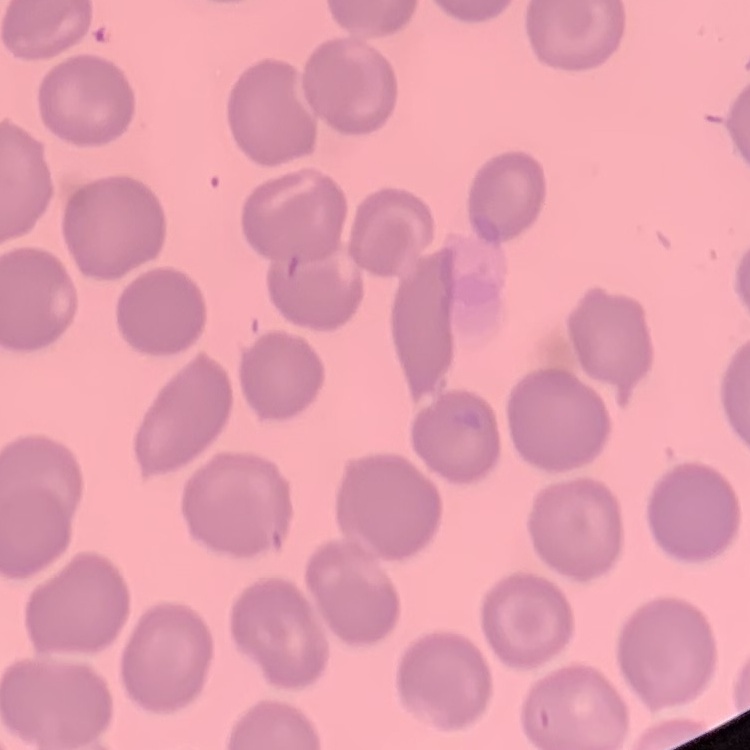

Summary:
  - Red blood cell morphology: no rouleaux formation
  - Stain: Field's or Giemsa
  - Preparation: thin peripheral smear
  - Image type: square crop of a larger photomicrograph